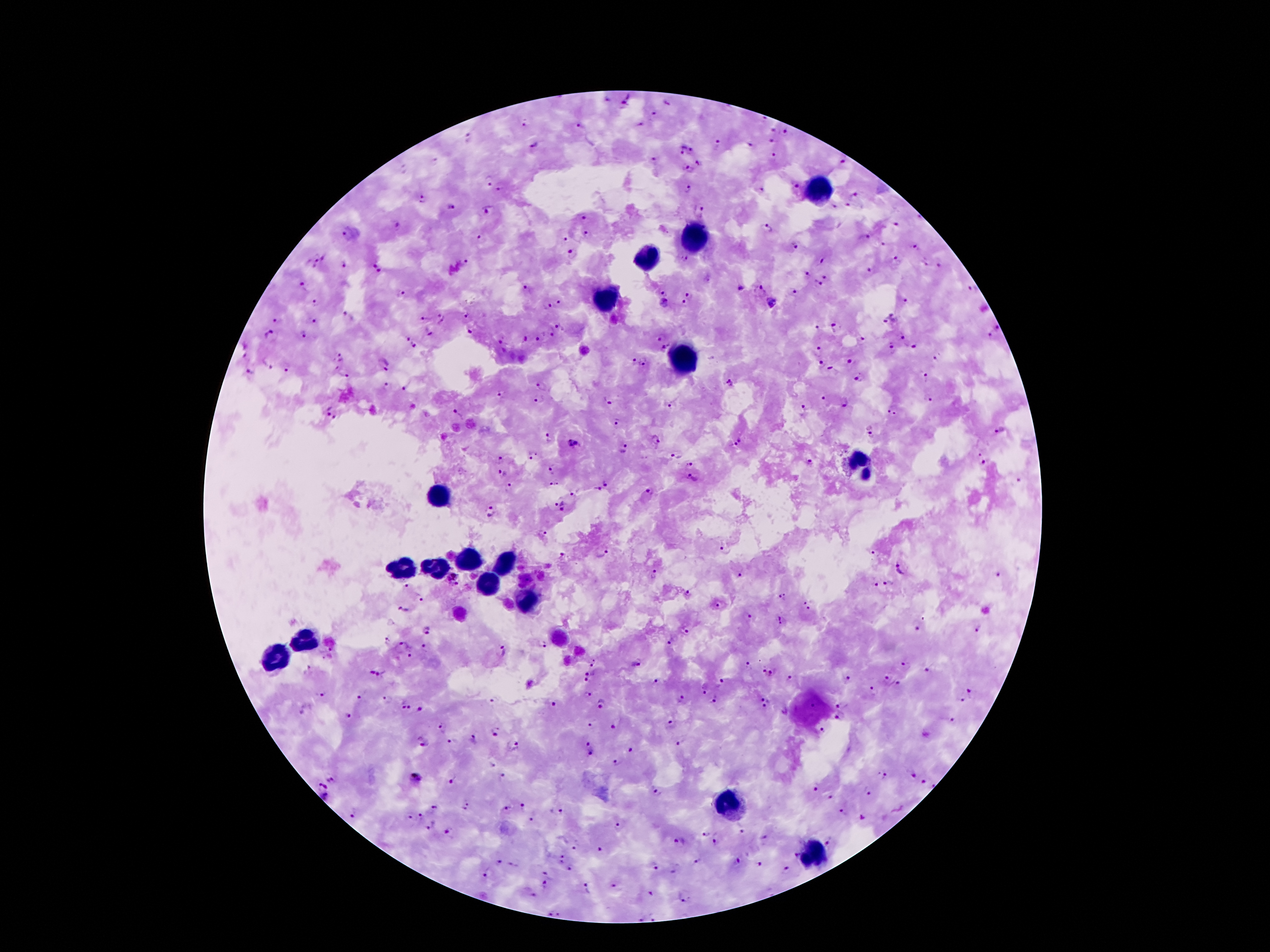

Approximate centers as (x, y) in pixels.
Summary:
  - Leukocyte locations: (819, 190), (695, 238), (646, 259), (606, 297), (683, 361), (861, 467), (440, 489), (463, 560), (501, 560), (403, 569), (431, 569), (489, 578), (530, 602), (308, 641), (273, 657), (729, 801), (814, 854)
  - Malaria parasite locations: (607, 100), (629, 100), (669, 103), (656, 113), (764, 118), (523, 124), (640, 125), (580, 127), (773, 131), (787, 131), (469, 137), (771, 141), (535, 146), (716, 146), (751, 146), (680, 149), (692, 151), (773, 156), (843, 160), (653, 161), (698, 163), (403, 168), (689, 168), (489, 181), (796, 186), (501, 189), (686, 189), (762, 189), (856, 195), (423, 199), (846, 205), (450, 208), (702, 209), (487, 210), (581, 217), (399, 224), (896, 224), (766, 227), (347, 233), (586, 235), (865, 237), (565, 238), (480, 239), (882, 244), (795, 245), (914, 245), (573, 253), (316, 256), (324, 257), (684, 258), (895, 259), (822, 260), (923, 262), (376, 263), (465, 263), (311, 265), (346, 265), (938, 265), (869, 271), (381, 272), (805, 275), (827, 278), (818, 284), (302, 285), (525, 288), (972, 289), (740, 290), (663, 291), (761, 292), (793, 292), (402, 293), (689, 293), (559, 301), (906, 301), (315, 302), (664, 303), (773, 303), (685, 304), (548, 305), (345, 314), (463, 315), (442, 318), (278, 319), (425, 319), (314, 320), (891, 320), (558, 326), (835, 327), (996, 327), (819, 328), (470, 332), (270, 333), (428, 333), (551, 333), (304, 335), (990, 336), (661, 337), (902, 337), (406, 339), (524, 339), (537, 340), (863, 340), (502, 341), (415, 345), (663, 347), (891, 347), (912, 347), (819, 351), (935, 356), (339, 357), (633, 361), (852, 361), (644, 363), (820, 363), (267, 365), (384, 365), (287, 369), (250, 370), (831, 370), (345, 375), (924, 375), (859, 379), (730, 383), (543, 384), (387, 386), (404, 388), (502, 394), (823, 399), (930, 399), (539, 400), (846, 401), (606, 402), (672, 406), (802, 409), (327, 411), (892, 411), (339, 415), (459, 415), (616, 423), (1000, 429), (870, 431), (547, 438), (655, 440), (737, 442), (572, 443), (623, 448), (978, 453), (531, 456), (675, 457), (500, 459), (690, 463), (811, 464), (983, 464), (551, 470), (502, 474), (694, 479), (1019, 481), (554, 483), (606, 483), (509, 488), (596, 490), (649, 492), (575, 493), (553, 500), (564, 507), (491, 511), (542, 533), (726, 550), (602, 553), (875, 553), (561, 556), (902, 569), (998, 574), (655, 575), (741, 576), (455, 580), (889, 583), (874, 585), (407, 587), (687, 594), (782, 597), (808, 599), (421, 600), (720, 605), (403, 608), (809, 609), (748, 617), (782, 621), (916, 629), (428, 630), (978, 630), (686, 631), (385, 640), (671, 641), (402, 645), (542, 645), (425, 647), (503, 651), (330, 653), (410, 656), (595, 664), (635, 664), (746, 666), (906, 666), (309, 668), (928, 670), (375, 672), (591, 673), (764, 673), (774, 674), (790, 678), (886, 678), (848, 680), (585, 681), (656, 681), (721, 683), (897, 685), (704, 690), (874, 690), (321, 692), (970, 693), (587, 694), (360, 697), (762, 697), (388, 699), (681, 699), (960, 700), (713, 701), (493, 702), (403, 704), (603, 704), (552, 706), (764, 706), (813, 706), (839, 706), (408, 708), (421, 710), (348, 717), (839, 717), (952, 722), (591, 725), (671, 725), (613, 726), (443, 727), (822, 730), (495, 732), (473, 738), (423, 741), (454, 742), (587, 743), (680, 744), (513, 746), (631, 749), (592, 754), (617, 762), (492, 765), (913, 775), (883, 776), (416, 778), (503, 778), (452, 780), (332, 781), (923, 781), (322, 786), (932, 786), (816, 788), (867, 791), (657, 793), (829, 797), (326, 798), (524, 806), (435, 807), (467, 807), (507, 809), (557, 812), (842, 812), (356, 813), (407, 816), (420, 816), (531, 818), (861, 818), (431, 826), (618, 826), (743, 830), (447, 831), (707, 832), (680, 840), (717, 840), (764, 840), (828, 842), (575, 848), (600, 849), (795, 857), (562, 859), (736, 861), (498, 862), (698, 862), (655, 865), (760, 865), (675, 868), (570, 869), (786, 869), (487, 874), (546, 874), (545, 883), (614, 886), (588, 888), (651, 893), (534, 896), (683, 896), (552, 913), (559, 913), (641, 916), (655, 916)
  - Stain: Giemsa
  - Patient malaria status: infected with Plasmodium falciparum
  - Magnification: 100x
  - Preparation: thick peripheral-blood smear
  - Capture: smartphone through the microscope eyepiece
  - Field of view: one from this slide
  - Image size: 1270×952 pixels